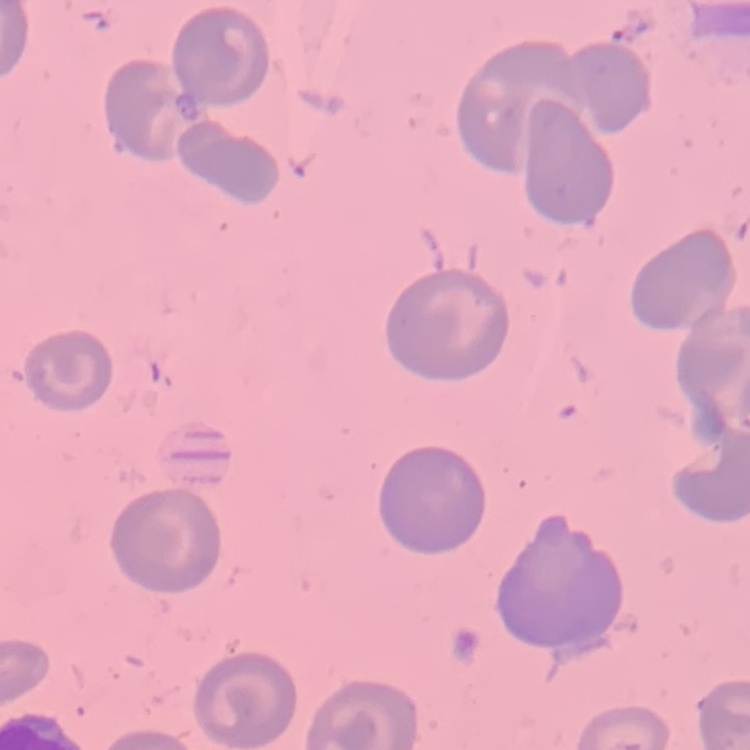
The erythrocytes exhibit no rouleaux formation. Thin blood film. Stained with either Field's or Giemsa. Square crop of a larger photomicrograph.